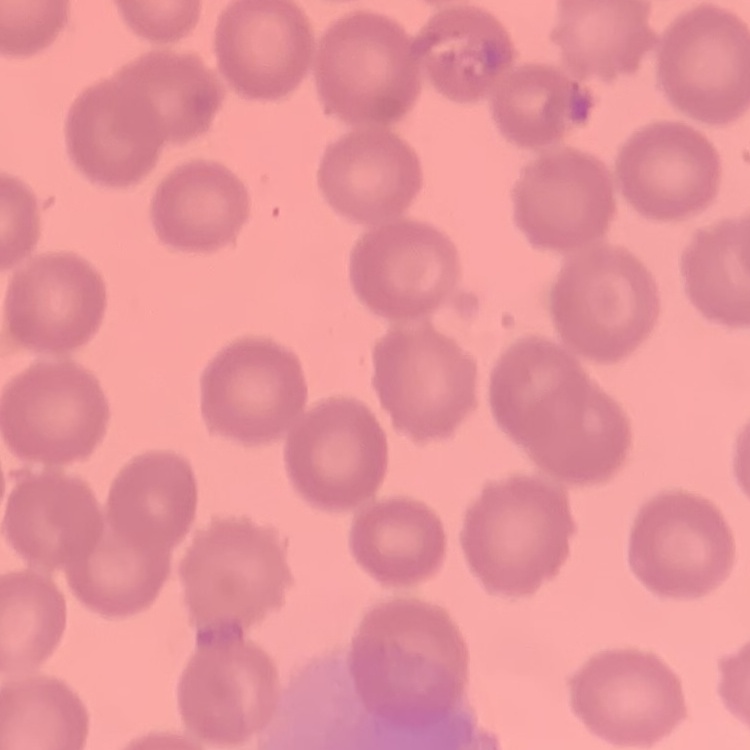

Summary:
  - Red blood cell morphology: no rouleaux formation
  - Preparation: thin peripheral smear
  - Image type: one tile cut from a larger photomicrograph
  - Stain: Field's or Giemsa